Describe the morphology of the red blood cells.
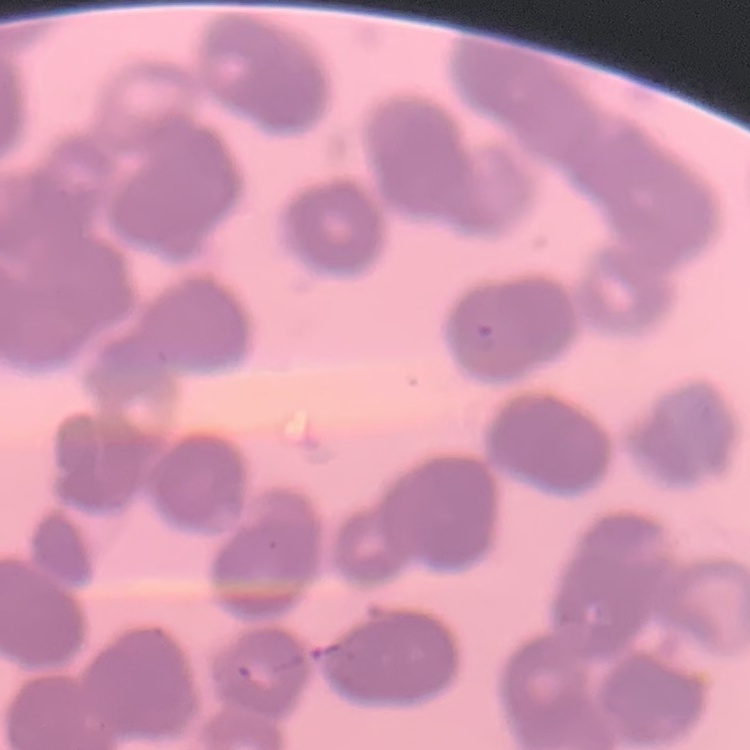
They show rouleaux formation.

Square crop of a larger photomicrograph. Field's or Giemsa stain. Thin blood smear.